Classify this cell by malaria status.
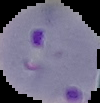
It is parasitized.

preparation = thin blood film
image type = segmented cell region with the area outside set to black
image size = 100×103 pixels